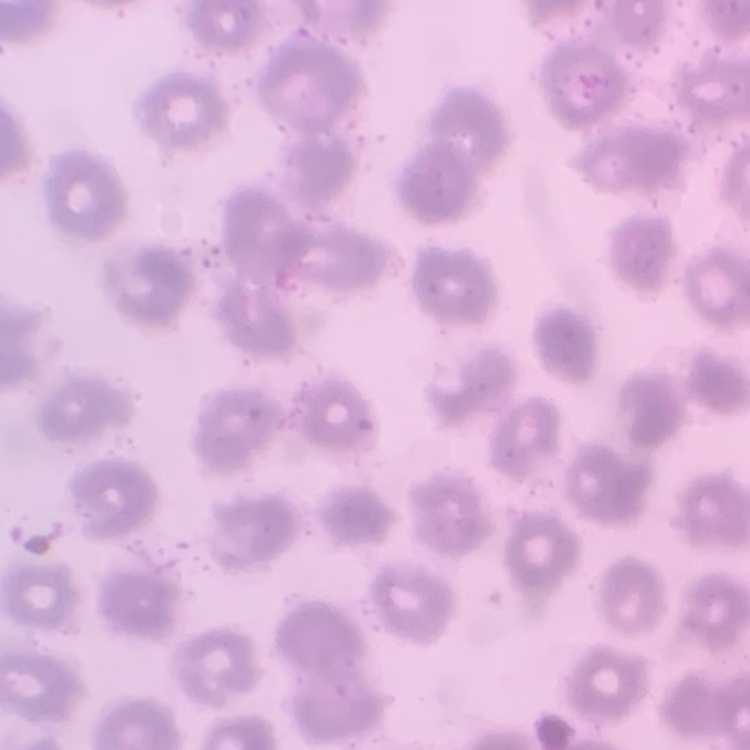
The erythrocytes exhibit no rouleaux formation. Square crop of a larger photomicrograph. Field's or Giemsa stain. Thin peripheral smear.